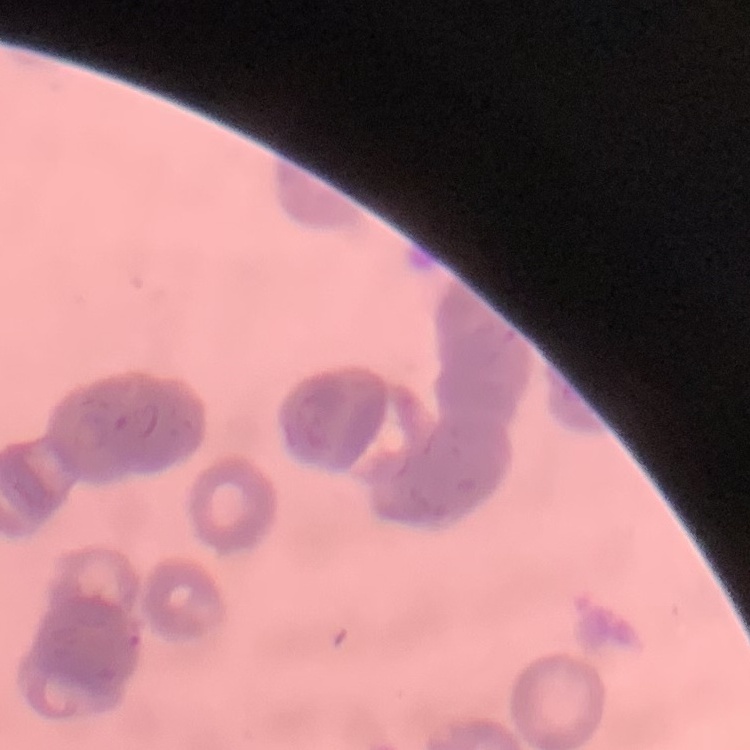
{
  "erythrocyte_morphology": "rouleaux formation",
  "stain": "Field's or Giemsa",
  "preparation": "thin blood film",
  "image_type": "square crop of a larger photomicrograph"
}